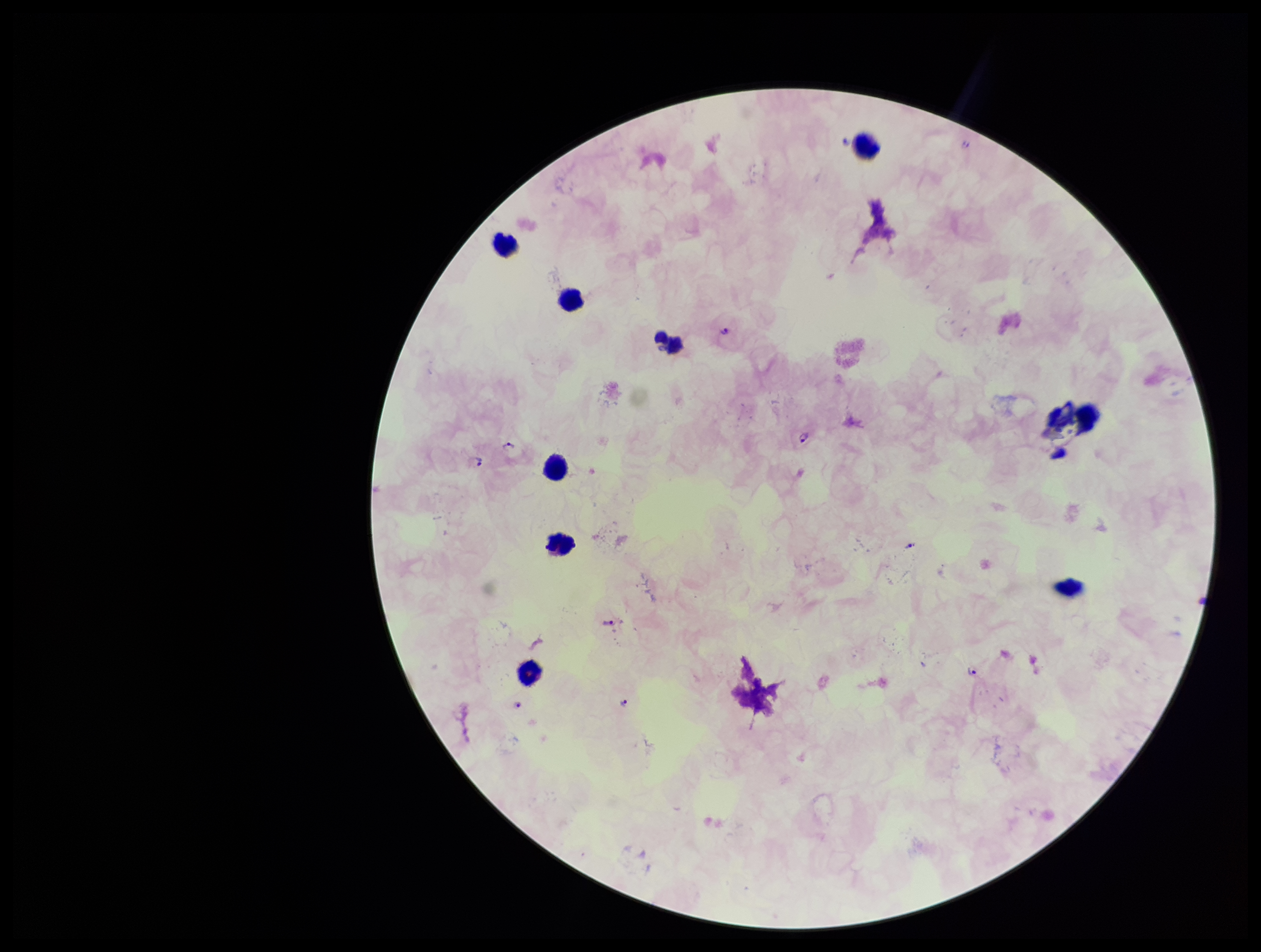
{
  "plasmodium_parasites": "seen",
  "leukocyte_count": 9,
  "field_of_view": "one from this slide",
  "parasite_count": 6,
  "preparation": "thick blood smear",
  "stain": "Giemsa",
  "patient_malaria_status": "infected",
  "image_size": "1261×952 pixels",
  "species_reported_for_this_patient": "Plasmodium falciparum",
  "capture": "smartphone photograph through the microscope eyepiece"
}